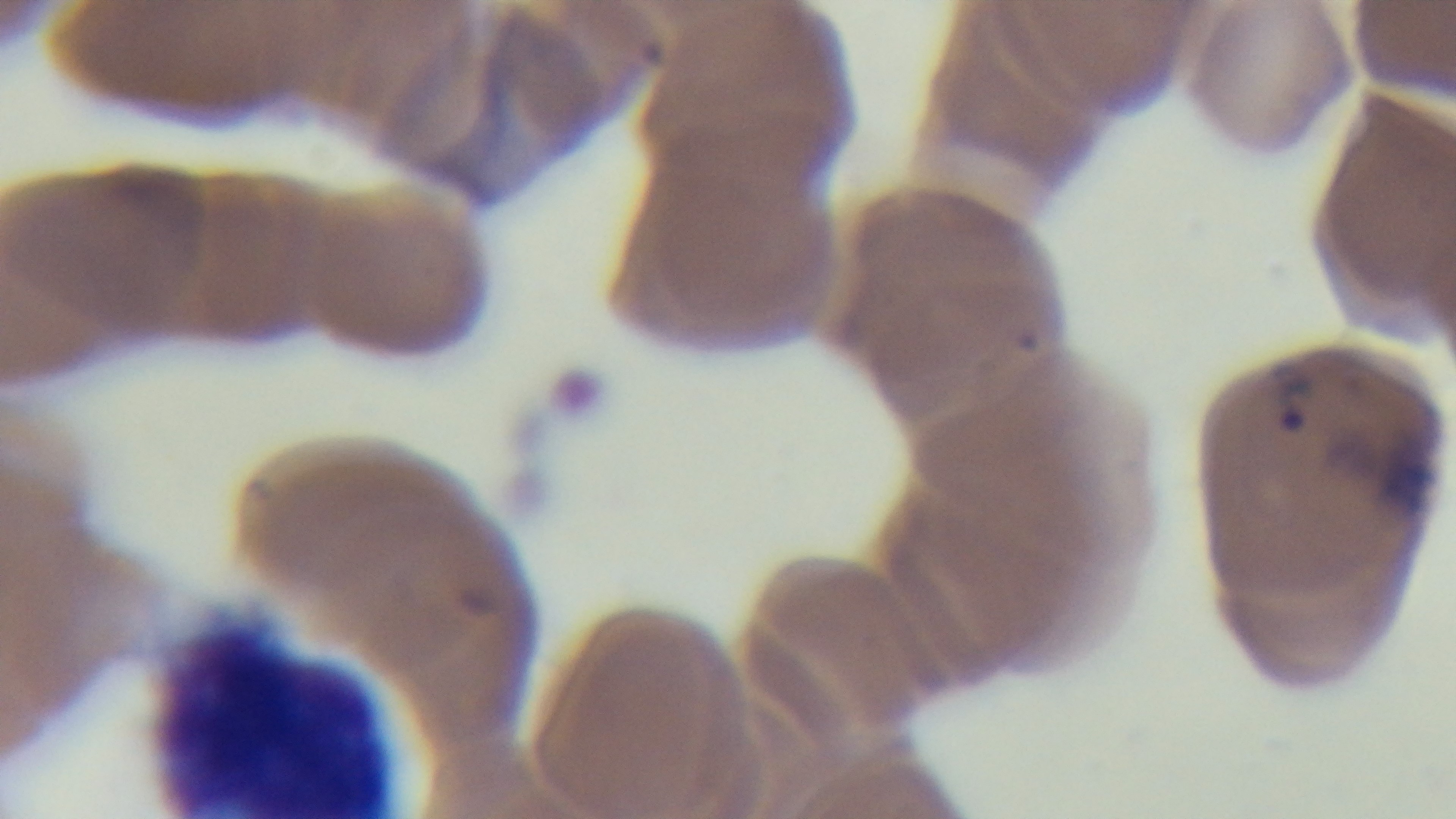

field of view = one from the slide
stain = Giemsa
objective = 100x oil immersion
malaria status = positive
modality = light microscopy
capture = mounted 4K digital camera
preparation = thin blood film